Name the blood parasite species.
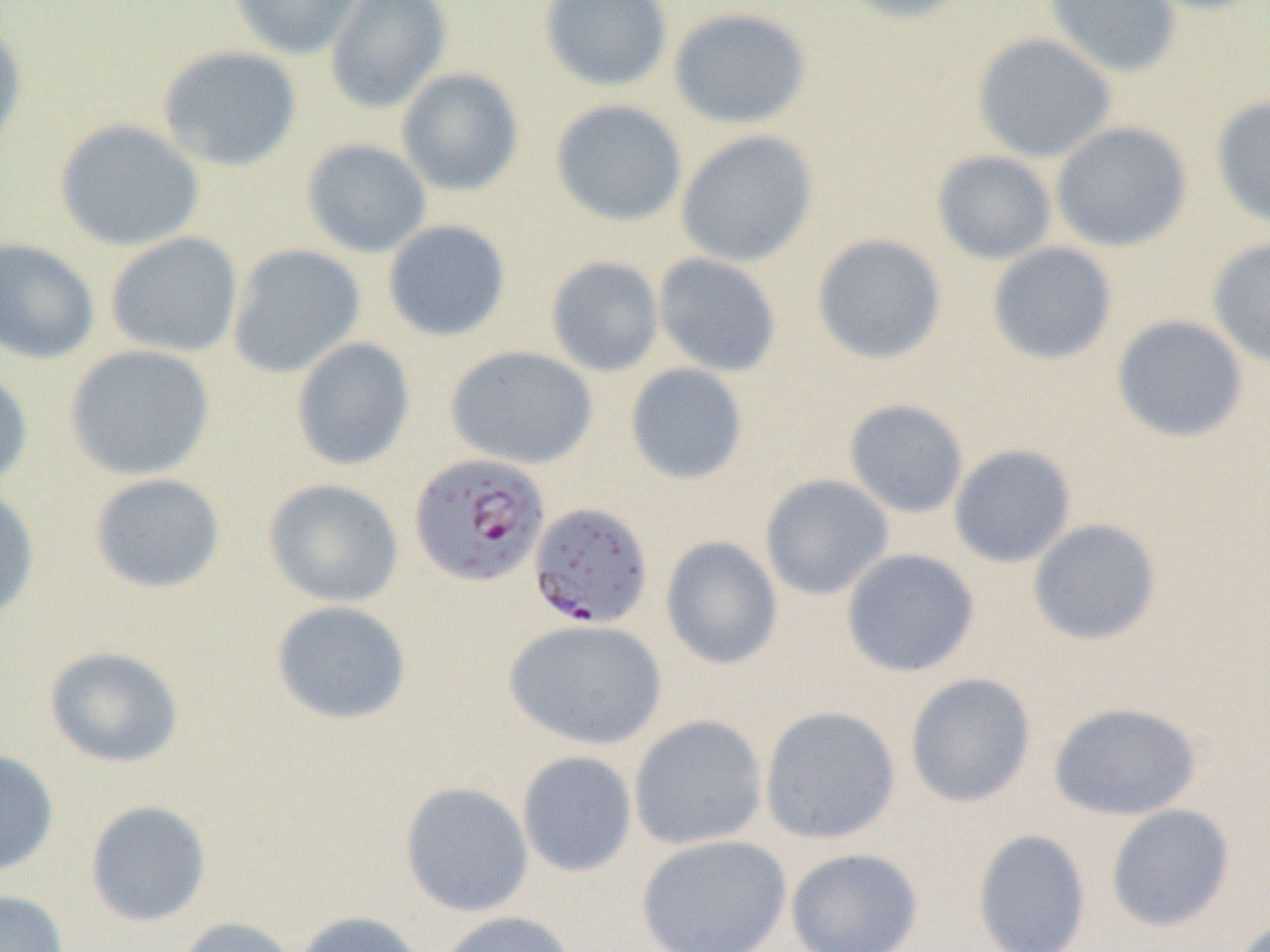

Plasmodium falciparum.

Approximate bounding boxes as (x1, y1, x2, y2) in pixels. Plasmodium falciparum-infected red blood cell locations: (409, 452, 551, 588), (528, 501, 654, 630). Uninfected red blood cell locations: (227, 0, 366, 59), (324, 0, 452, 115), (539, 0, 673, 92), (836, 0, 976, 24), (1044, 0, 1182, 78), (1131, 0, 1270, 16), (667, 6, 812, 130), (0, 17, 28, 164), (971, 32, 1117, 164), (157, 45, 302, 172), (396, 67, 524, 196), (1210, 95, 1270, 229), (550, 99, 688, 228), (53, 118, 204, 252), (1050, 121, 1193, 252), (676, 129, 819, 268), (301, 138, 432, 258), (931, 150, 1057, 266), (382, 219, 512, 343), (105, 231, 243, 359), (811, 233, 947, 365), (0, 237, 100, 364), (1206, 237, 1270, 368), (986, 241, 1118, 366), (227, 243, 365, 378), (652, 252, 782, 378), (545, 256, 665, 377), (1111, 314, 1249, 444), (290, 337, 415, 472), (63, 344, 215, 481), (445, 345, 599, 470), (624, 362, 749, 485), (0, 365, 34, 493), (843, 398, 970, 518), (948, 444, 1077, 568), (88, 472, 226, 594), (759, 473, 895, 601), (263, 478, 404, 607), (0, 485, 40, 622), (1027, 518, 1162, 646), (660, 536, 784, 670), (840, 548, 980, 678), (270, 599, 412, 726), (503, 618, 668, 751), (43, 645, 185, 768), (904, 672, 1037, 808), (1047, 701, 1202, 821), (759, 705, 902, 844), (629, 714, 768, 851), (0, 748, 60, 878), (516, 750, 638, 877), (399, 781, 534, 918), (84, 799, 212, 927), (1105, 803, 1236, 933), (971, 828, 1092, 952), (636, 833, 792, 952), (785, 847, 924, 952), (0, 889, 69, 952), (292, 909, 428, 952), (434, 910, 578, 952), (174, 915, 300, 952), (1229, 915, 1269, 952). Image is 1270×952 pixels. Optical microscopy. 1000x magnification. Thin blood film. Single field of view.